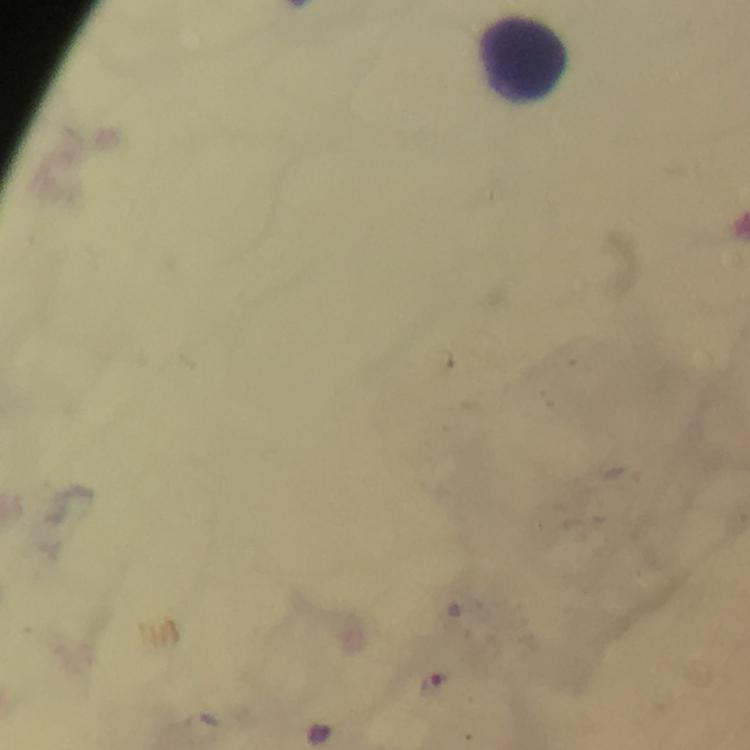
Approximate object centers, in pixels from the top-left corner. Leukocyte locations: (x=526, y=58). Malaria parasite locations: (x=434, y=683). Giemsa stain. Thick blood smear. Immersion oil was used. 100x magnification. From a malaria diagnostic workup. A crop from one field of view. Smartphone photograph taken through a microscope. Image is 750×750 pixels.